Locate every malaria parasite.
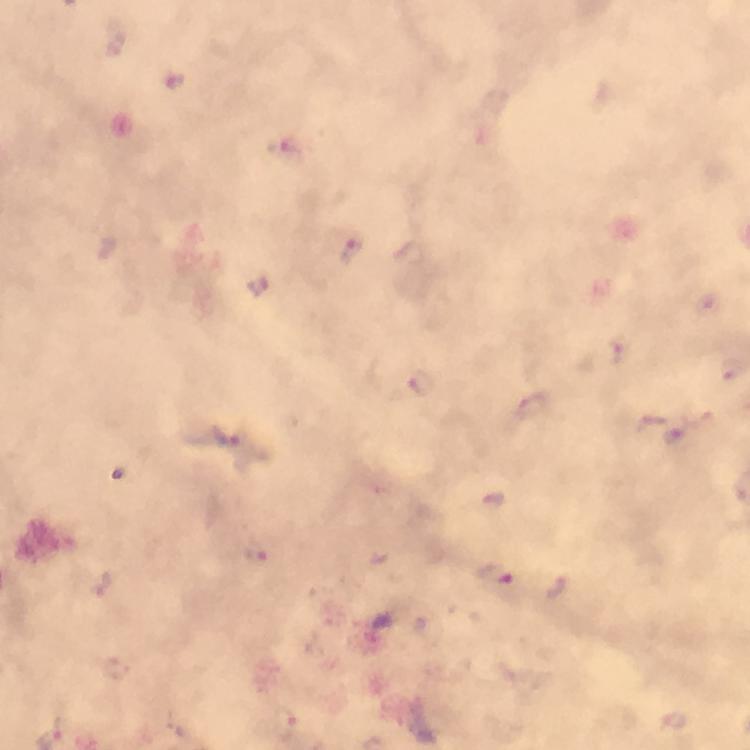

Approximate object centers, in pixels from the top-left corner.
Malaria parasites: (x=176, y=80), (x=350, y=252), (x=409, y=252), (x=260, y=286), (x=707, y=304), (x=618, y=352), (x=424, y=383), (x=535, y=406), (x=650, y=422), (x=229, y=437), (x=493, y=576), (x=558, y=587).

Summary:
  - Immersion oil: used
  - Magnification: 100x
  - Preparation: thick blood film
  - Capture: smartphone mounted on the microscope
  - Cropped from: one field of view
  - Context: from a diagnostic examination for malaria
  - Stain: Giemsa
  - Image size: 750×750 pixels